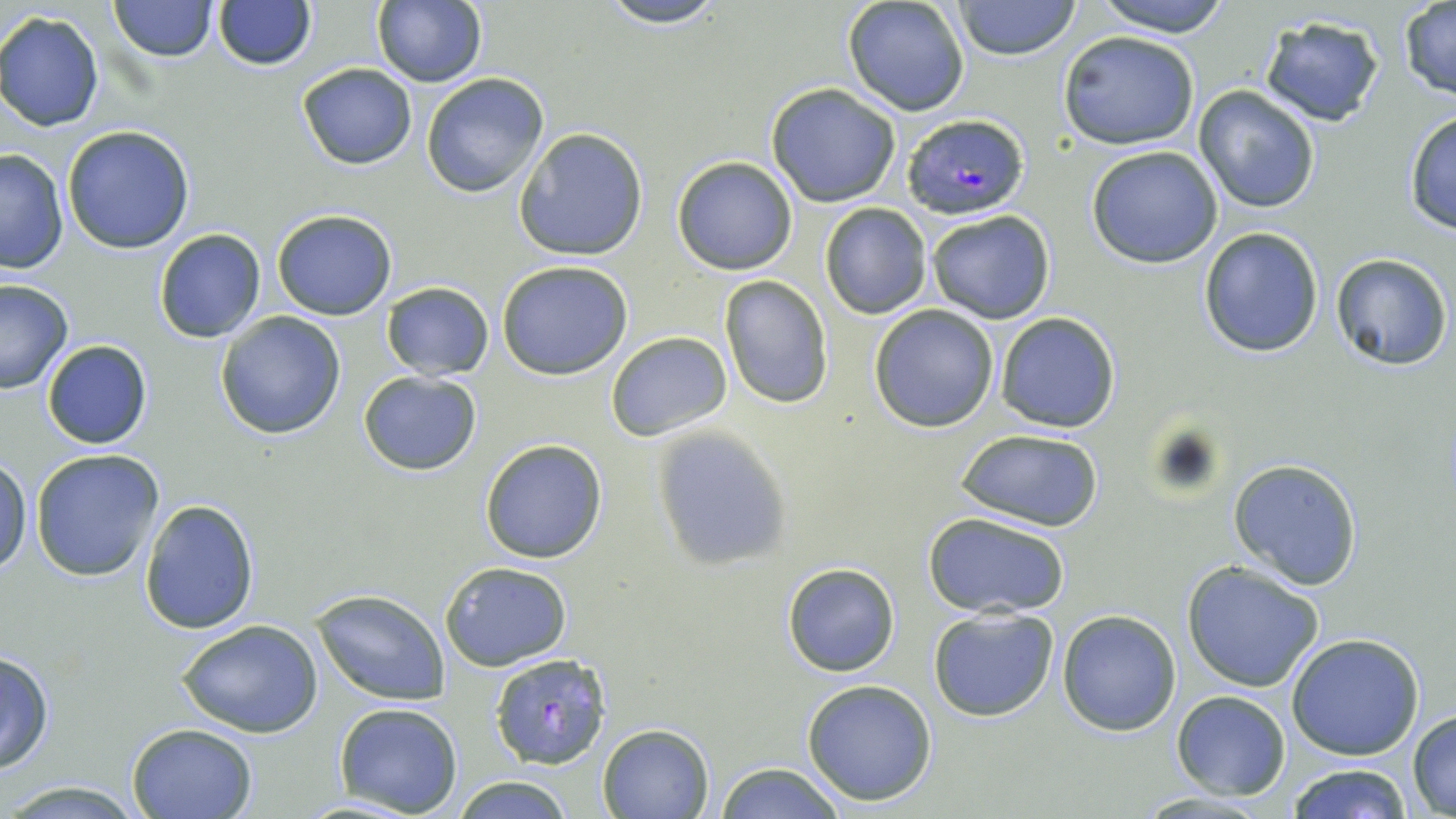
slide-level diagnosis = Plasmodium falciparum
image size = 1456×819 pixels
uninfected red blood cell locations = approximate bounding boxes as [x1, y1, x2, y2] in pixels: [109, 0, 216, 61], [372, 0, 486, 87], [594, 0, 732, 28], [840, 0, 971, 116], [954, 0, 1079, 61], [1092, 0, 1235, 37], [213, 2, 315, 70], [1398, 2, 1456, 99], [0, 12, 104, 131], [1257, 14, 1387, 129], [1058, 30, 1200, 151], [297, 62, 416, 169], [421, 73, 549, 197], [765, 82, 902, 207], [1193, 84, 1323, 214], [1402, 109, 1455, 234], [61, 125, 194, 253], [512, 128, 649, 262], [1085, 145, 1224, 267], [0, 149, 69, 274], [671, 156, 798, 274], [818, 202, 933, 320], [272, 207, 397, 320], [925, 209, 1056, 325], [1198, 226, 1325, 359], [154, 229, 267, 343], [1330, 253, 1452, 370], [496, 259, 634, 379], [719, 275, 833, 408], [1, 278, 73, 394], [379, 282, 495, 380], [867, 303, 1000, 432], [215, 311, 346, 440], [993, 311, 1120, 434], [605, 331, 732, 442], [41, 339, 152, 450], [358, 371, 482, 475], [647, 424, 794, 571], [954, 426, 1107, 530], [479, 438, 608, 565], [31, 449, 166, 581], [0, 452, 32, 575], [1230, 457, 1363, 589], [140, 497, 260, 634], [925, 512, 1071, 619], [439, 560, 573, 672], [1182, 562, 1324, 691], [781, 563, 900, 677], [311, 591, 448, 706], [927, 606, 1060, 722], [1057, 609, 1182, 736], [177, 620, 323, 738], [1285, 633, 1427, 759], [0, 649, 55, 774], [802, 679, 938, 806], [1171, 691, 1290, 799], [334, 701, 463, 816], [1407, 710, 1456, 815], [126, 722, 258, 818], [597, 723, 715, 818], [713, 763, 847, 819], [1285, 763, 1414, 818], [451, 775, 577, 819], [0, 779, 152, 818]
Plasmodium falciparum-infected red blood cell locations = approximate bounding boxes as [x1, y1, x2, y2] in pixels: [901, 113, 1030, 220], [490, 652, 612, 771]
preparation = thin blood film
field of view = one of a larger specimen
modality = optical microscopy
stain = May-Grünwald-Giemsa
magnification = 1000x